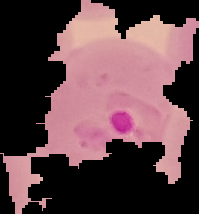
Summary:
  - Image size: 199×214 pixels
  - Image type: segmented cell region with the area outside set to black
  - Malaria status: parasitized
  - Preparation: thin blood film